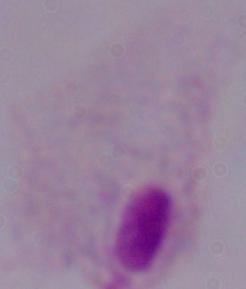

Photomicrograph. A trichomonad is shown. 1000x magnification.